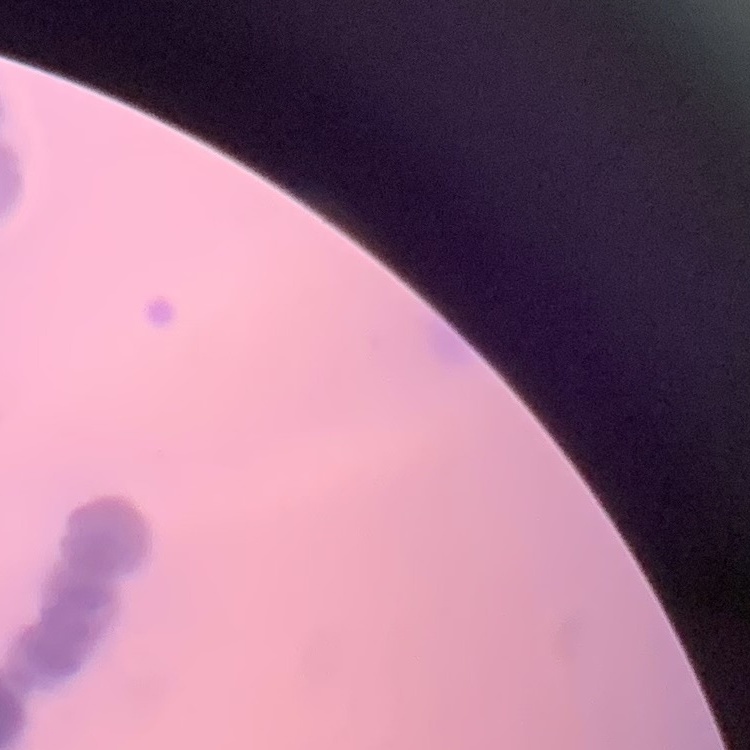

Summary:
  - Red blood cell morphology: rouleaux formation
  - Stain: Field's or Giemsa
  - Preparation: thin blood film
  - Image type: square crop of a larger photomicrograph